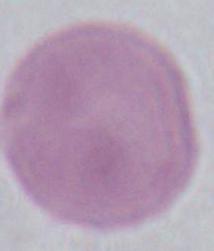 Photomicrograph. Captured at 1000x magnification. An erythrocyte is seen.